Report the malaria status of this cell.
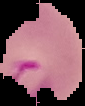
It is parasitized.

Summary:
  - Preparation: thin blood film
  - Image size: 85×106 pixels
  - Image type: segmented cell region on a black background